Locate and identify every blood parasite.
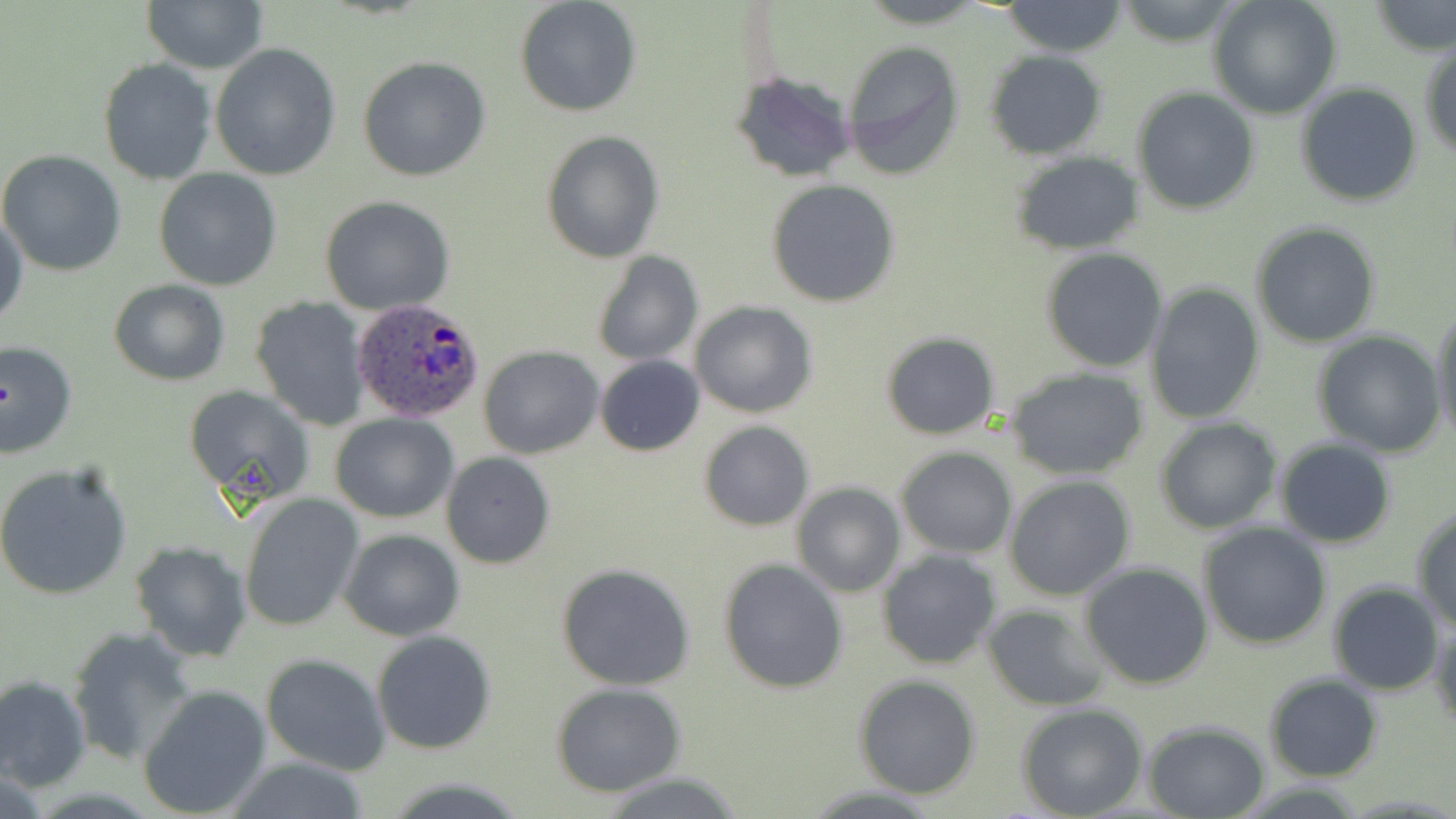
Approximate bounding boxes as [x1, y1, x2, y2] in pixels.
Plasmodium ovale-infected red blood cells: [353, 298, 487, 423].
No Plasmodium falciparum, Plasmodium malariae, Plasmodium vivax, Babesia divergens, or Trypanosoma brucei observed.

Summary:
  - Uninfected red blood cell locations: [141, 0, 269, 72], [514, 0, 642, 118], [1207, 0, 1342, 119], [1373, 0, 1456, 55], [1000, 1, 1129, 58], [1107, 2, 1249, 45], [1419, 36, 1456, 160], [839, 39, 964, 177], [211, 42, 342, 180], [984, 51, 1108, 160], [357, 55, 491, 182], [98, 58, 215, 184], [728, 71, 854, 182], [1295, 82, 1423, 206], [1133, 88, 1259, 214], [542, 129, 666, 263], [0, 151, 127, 276], [1009, 151, 1144, 255], [154, 169, 283, 290], [765, 179, 901, 307], [320, 197, 457, 314], [0, 211, 26, 331], [1250, 222, 1382, 349], [1040, 247, 1169, 372], [591, 251, 703, 367], [108, 278, 229, 386], [1144, 280, 1267, 426], [249, 297, 372, 432], [691, 301, 818, 418], [1429, 303, 1455, 453], [1312, 331, 1447, 458], [880, 332, 1001, 441], [0, 340, 76, 460], [478, 347, 603, 460], [596, 356, 704, 456], [1005, 366, 1149, 480], [182, 384, 314, 505], [331, 413, 459, 523], [1155, 417, 1281, 534], [697, 421, 814, 532], [1273, 438, 1396, 549], [896, 447, 1018, 559], [441, 451, 555, 569], [0, 460, 134, 601], [1005, 475, 1136, 599], [792, 483, 905, 598], [238, 493, 364, 632], [1410, 505, 1456, 634], [1197, 522, 1334, 650], [339, 529, 465, 642], [129, 540, 252, 662], [876, 549, 1002, 668], [718, 558, 848, 694], [1079, 560, 1213, 689], [555, 561, 699, 691], [1326, 583, 1445, 695], [982, 601, 1111, 712], [1430, 611, 1456, 733], [67, 627, 196, 768], [371, 631, 496, 754], [260, 654, 391, 774], [0, 674, 93, 793], [853, 674, 983, 799], [1264, 675, 1382, 782], [550, 682, 689, 798], [138, 686, 274, 818], [1015, 703, 1148, 819], [1141, 721, 1271, 818], [220, 757, 376, 818], [596, 772, 749, 817]
  - Slide-level diagnosis: Plasmodium ovale
  - Magnification: 1000x
  - Modality: light microscopy
  - Image size: 1456×819 pixels
  - Field of view: single
  - Stain: May-Grünwald-Giemsa
  - Preparation: thin blood smear